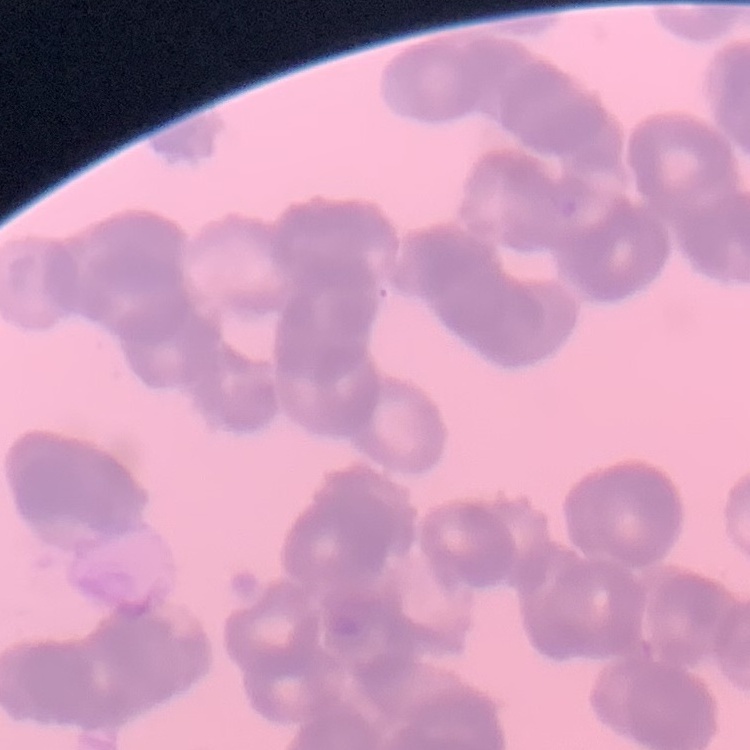

Summary:
  - Red blood cell morphology: rouleaux formation
  - Stain: Field's or Giemsa
  - Image type: square crop of a larger photomicrograph
  - Preparation: thin peripheral smear